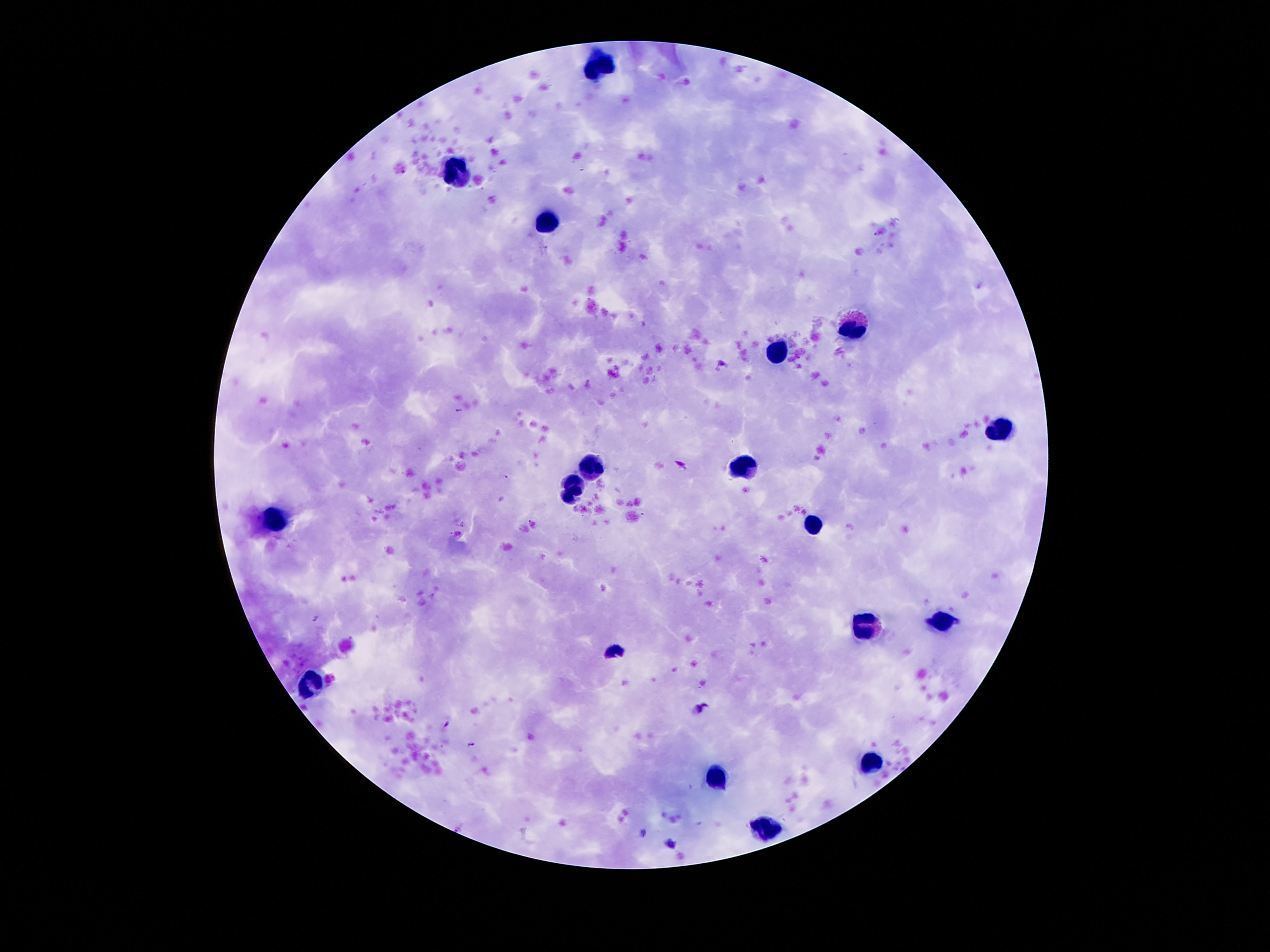
Approximate centers as (x, y) in pixels. Leukocyte locations: (602, 67), (456, 177), (548, 225), (850, 329), (772, 351), (998, 431), (592, 465), (744, 465), (572, 489), (276, 519), (810, 527), (944, 623), (862, 627), (312, 683), (870, 759), (714, 779), (766, 829). Thick blood film. Image is 1270×952 pixels. Photographed through the microscope eyepiece with a smartphone camera. Single field of view. 100x magnification. Giemsa stain. Patient malaria status: not infected.